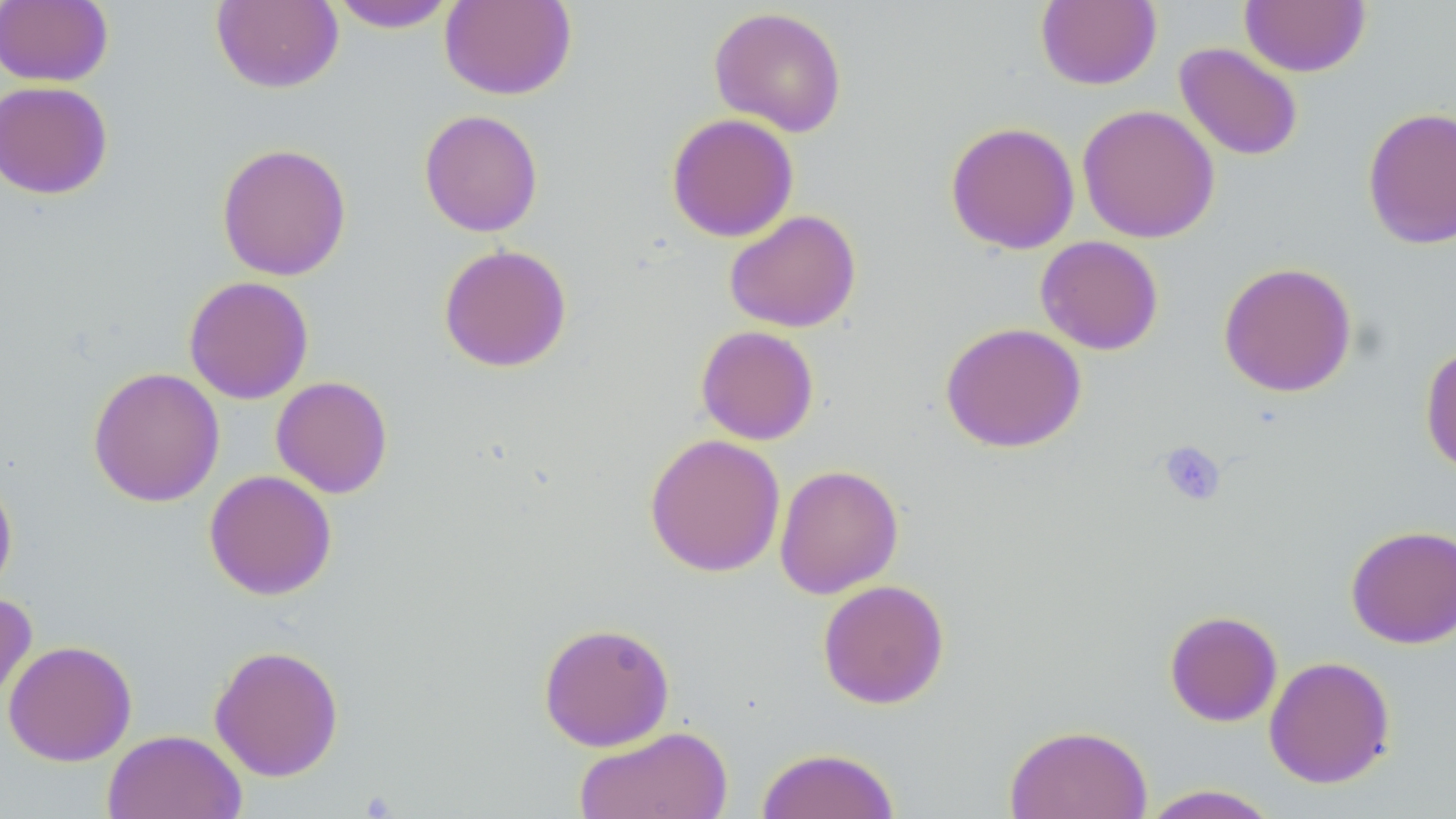 Approximate bounding boxes as named x1/y1/x2/y2 corners in pixels. Platelet locations: (x1=1158, y1=440, x2=1227, y2=506). Uninfected red blood cell locations: (x1=327, y1=0, x2=460, y2=32), (x1=0, y1=1, x2=113, y2=87), (x1=210, y1=1, x2=344, y2=93), (x1=439, y1=1, x2=577, y2=100), (x1=1035, y1=1, x2=1162, y2=90), (x1=1239, y1=1, x2=1371, y2=77), (x1=709, y1=6, x2=848, y2=137), (x1=1174, y1=42, x2=1304, y2=162), (x1=0, y1=80, x2=113, y2=200), (x1=1077, y1=104, x2=1220, y2=244), (x1=1362, y1=105, x2=1456, y2=250), (x1=419, y1=109, x2=544, y2=237), (x1=666, y1=112, x2=799, y2=242), (x1=945, y1=121, x2=1080, y2=254), (x1=216, y1=142, x2=352, y2=281), (x1=724, y1=210, x2=862, y2=333), (x1=1035, y1=235, x2=1164, y2=355), (x1=438, y1=244, x2=572, y2=373), (x1=1218, y1=261, x2=1357, y2=397), (x1=183, y1=276, x2=314, y2=404), (x1=940, y1=322, x2=1086, y2=453), (x1=696, y1=325, x2=819, y2=445), (x1=1419, y1=344, x2=1456, y2=476), (x1=87, y1=366, x2=225, y2=507), (x1=271, y1=376, x2=393, y2=498), (x1=644, y1=433, x2=785, y2=577), (x1=774, y1=464, x2=904, y2=599), (x1=203, y1=469, x2=337, y2=600), (x1=0, y1=471, x2=18, y2=600), (x1=1345, y1=524, x2=1456, y2=649), (x1=817, y1=579, x2=950, y2=709), (x1=0, y1=590, x2=37, y2=708), (x1=1164, y1=610, x2=1283, y2=727), (x1=538, y1=621, x2=675, y2=752), (x1=2, y1=639, x2=137, y2=766), (x1=208, y1=643, x2=344, y2=782), (x1=1264, y1=656, x2=1396, y2=789), (x1=1004, y1=723, x2=1152, y2=819), (x1=574, y1=725, x2=733, y2=819), (x1=103, y1=729, x2=247, y2=819), (x1=756, y1=747, x2=901, y2=819), (x1=1139, y1=784, x2=1281, y2=819). Slide-level diagnosis: negative for blood parasites. Single field of view. Captured at 1000x magnification. Thin blood film. May-Grünwald-Giemsa stain. Light microscopy. Image is 1456×819 pixels.